Name the blood parasite species.
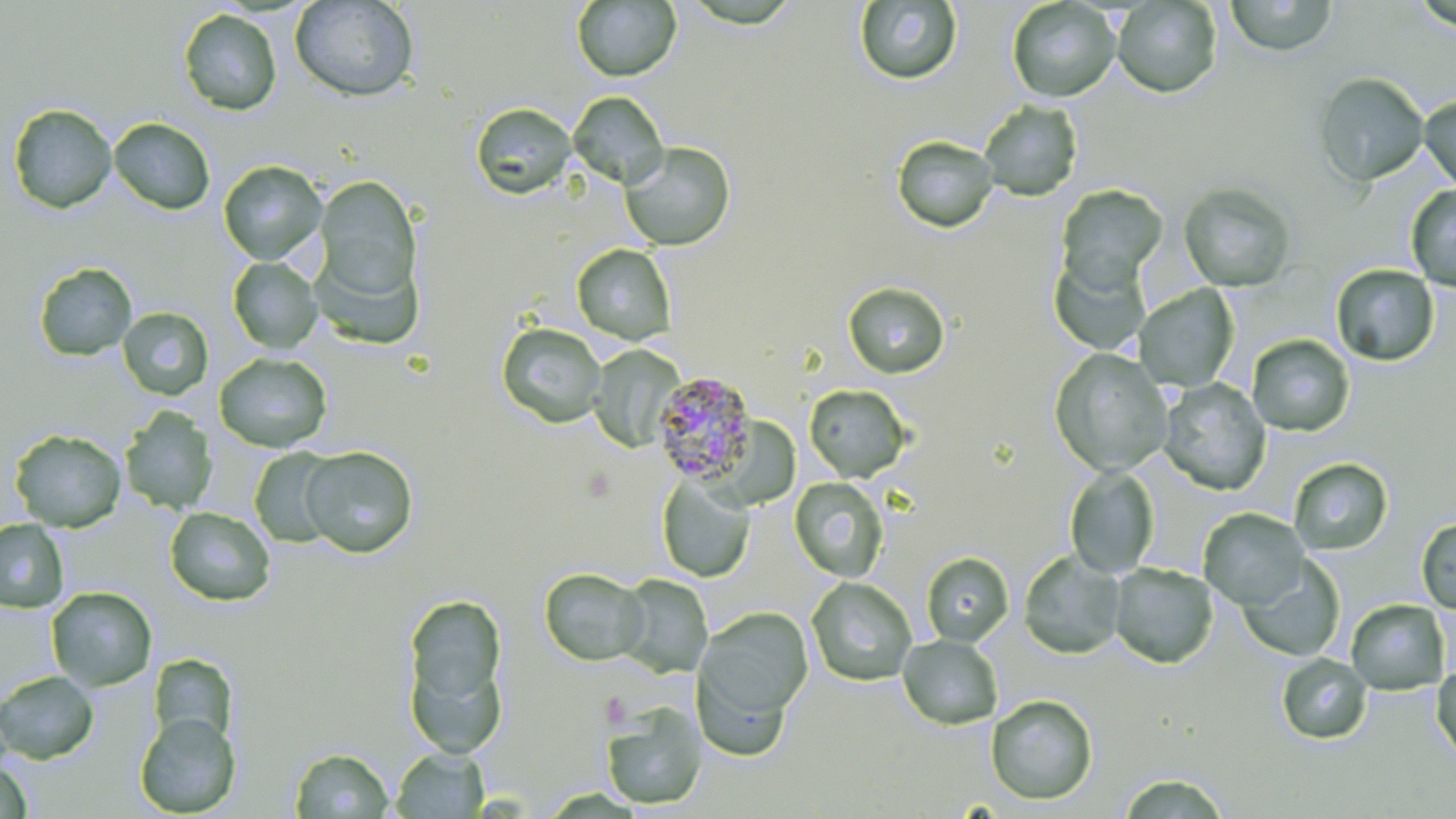

Plasmodium malariae.

Summary:
  - Coordinate format: approximate bounding boxes as [x1, y1, x2, y2] in pixels
  - Plasmodium malariae-infected red blood cell locations: [651, 371, 758, 485]
  - Platelet locations: [599, 692, 633, 728]
  - Uninfected red blood cell locations: [290, 0, 419, 102], [1005, 0, 1121, 103], [1224, 0, 1338, 57], [571, 1, 681, 82], [854, 1, 963, 85], [1111, 1, 1223, 98], [178, 9, 282, 116], [1313, 72, 1428, 186], [568, 92, 669, 189], [1419, 94, 1456, 193], [979, 100, 1083, 201], [471, 102, 577, 200], [7, 103, 117, 214], [109, 118, 216, 215], [891, 135, 999, 233], [620, 141, 736, 252], [218, 160, 328, 265], [314, 173, 423, 317], [1177, 182, 1297, 292], [1055, 184, 1168, 291], [1405, 185, 1456, 290], [572, 245, 677, 345], [1048, 255, 1152, 356], [228, 257, 322, 354], [33, 262, 137, 362], [1330, 264, 1440, 366], [843, 281, 950, 378], [1133, 284, 1240, 392], [117, 307, 214, 400], [497, 322, 606, 428], [1246, 334, 1356, 437], [588, 345, 684, 453], [1049, 348, 1173, 477], [214, 353, 332, 453], [1159, 378, 1270, 495], [803, 384, 912, 483], [120, 409, 219, 515], [9, 428, 127, 532], [299, 445, 419, 558], [248, 448, 342, 548], [1289, 458, 1394, 555], [1064, 465, 1161, 579], [657, 474, 756, 583], [789, 477, 889, 582], [797, 478, 896, 685], [165, 507, 276, 607], [1198, 508, 1310, 610], [1415, 517, 1456, 613], [0, 518, 70, 614], [1018, 550, 1126, 659], [921, 551, 1014, 646], [1237, 557, 1346, 662], [1108, 562, 1219, 669], [538, 567, 649, 666], [617, 575, 712, 678], [806, 577, 917, 686], [46, 586, 157, 692], [401, 591, 510, 741], [1346, 599, 1451, 695], [698, 607, 813, 723], [897, 634, 1003, 730], [148, 653, 238, 747], [1276, 653, 1372, 744], [693, 663, 793, 762], [1430, 663, 1456, 764], [0, 670, 99, 764], [985, 694, 1099, 806], [600, 700, 707, 810], [135, 712, 241, 817], [289, 746, 394, 818], [390, 747, 490, 818], [1, 760, 33, 819], [1117, 772, 1234, 817]
  - Preparation: thin blood smear
  - Stain: May-Grünwald-Giemsa
  - Magnification: 1000x
  - Modality: optical microscopy
  - Field of view: one of a larger specimen
  - Image size: 1456×819 pixels